State which parasite is depicted.
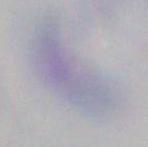
This is Toxoplasma gondii.

modality = micrograph
magnification = 1000x